Name the parasite shown.
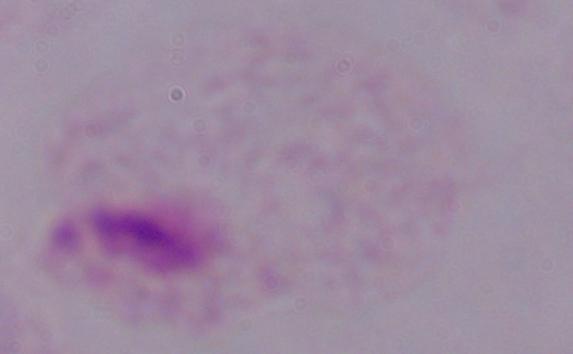
This is a trichomonad.

Micrograph. Captured at 1000x magnification.